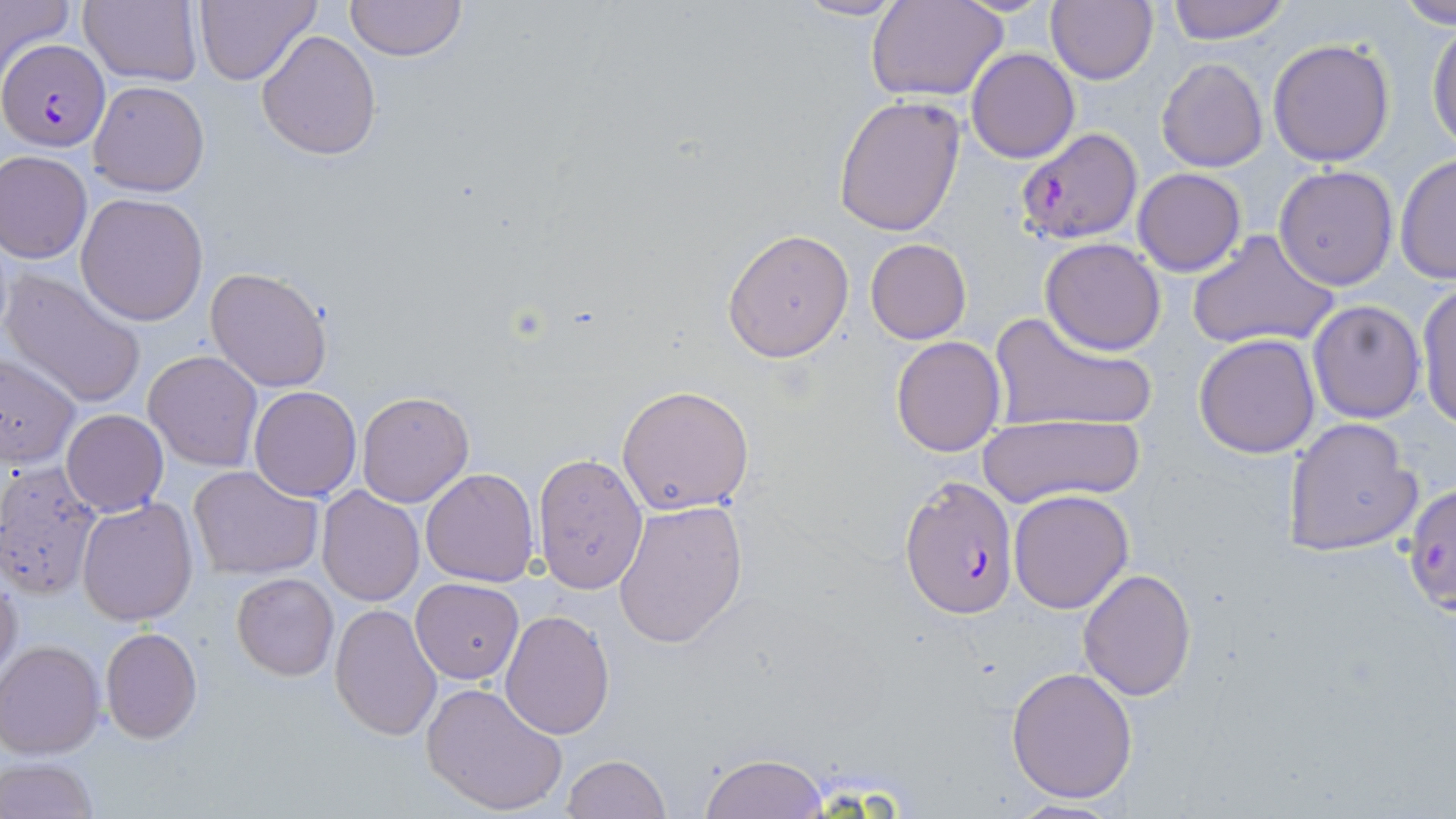

slide-level diagnosis = Plasmodium falciparum
stain = May-Grünwald-Giemsa
modality = optical microscopy
Plasmodium falciparum-infected red blood cell locations = approximate bounding boxes as [x1, y1, x2, y2] in pixels: [0, 39, 110, 152], [1015, 126, 1143, 245], [899, 476, 1018, 618], [1401, 482, 1456, 618]
uninfected red blood cell locations = approximate bounding boxes as [x1, y1, x2, y2] in pixels: [0, 0, 73, 75], [78, 0, 202, 87], [196, 0, 322, 87], [343, 0, 468, 63], [793, 0, 911, 22], [867, 0, 1008, 101], [1046, 0, 1158, 84], [1164, 0, 1292, 44], [1394, 1, 1456, 27], [1427, 23, 1456, 155], [256, 30, 382, 159], [1267, 38, 1396, 167], [967, 48, 1079, 163], [1156, 58, 1269, 172], [89, 80, 209, 197], [833, 95, 966, 237], [0, 150, 92, 263], [1395, 155, 1455, 284], [1274, 164, 1399, 290], [1132, 168, 1247, 277], [76, 192, 208, 326], [721, 227, 855, 362], [1186, 231, 1339, 352], [1039, 237, 1166, 355], [865, 238, 971, 344], [204, 267, 332, 392], [1, 268, 149, 409], [1415, 281, 1456, 428], [1308, 300, 1426, 423], [989, 309, 1156, 437], [1194, 334, 1322, 458], [891, 335, 1006, 457], [144, 350, 262, 470], [0, 354, 82, 470], [616, 385, 754, 516], [248, 387, 361, 500], [357, 390, 473, 507], [61, 409, 168, 517], [983, 414, 1143, 505], [1280, 418, 1423, 558], [532, 453, 648, 594], [0, 461, 103, 600], [187, 464, 323, 580], [421, 467, 540, 587], [317, 486, 424, 606], [1007, 490, 1134, 612], [77, 496, 201, 626], [612, 498, 748, 650], [0, 567, 23, 691], [1078, 568, 1196, 700], [231, 572, 339, 680], [411, 578, 524, 682], [330, 602, 442, 740], [500, 610, 614, 739], [99, 627, 202, 744], [1, 641, 104, 758], [1005, 666, 1138, 804], [421, 681, 568, 817], [562, 754, 669, 819], [700, 754, 828, 819], [1, 755, 101, 819], [1001, 799, 1129, 817]
field of view = single
image size = 1456×819 pixels
preparation = thin blood film
magnification = 1000x